Assess for Plasmodium parasites.
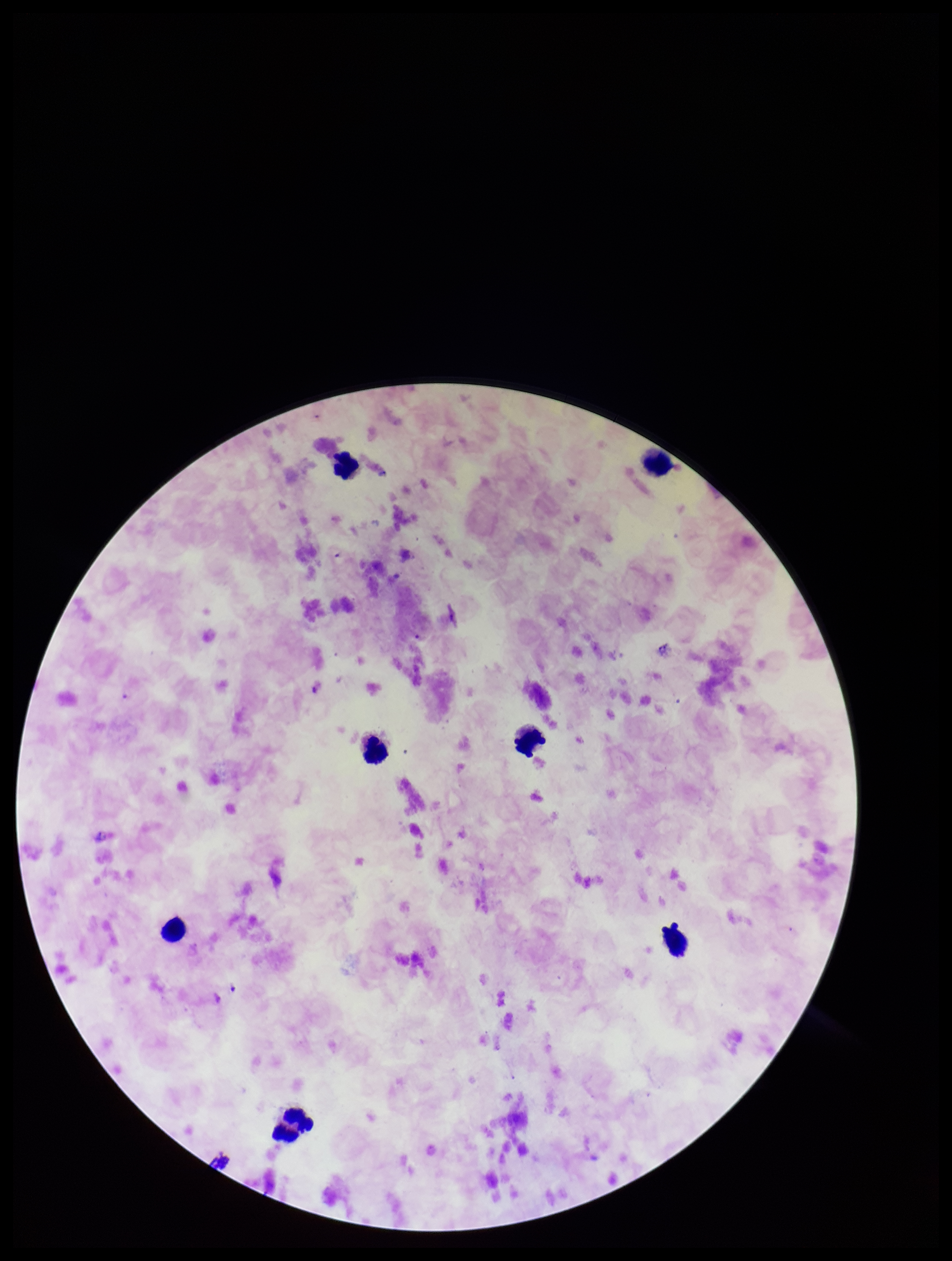

None identified.

Summary:
  - Capture: smartphone photograph through the microscope eyepiece
  - Patient malaria status: infected
  - Parasite count: 0
  - Stain: Giemsa
  - Leukocyte count: 7
  - Field of view: one from this slide
  - Image size: 952×1261 pixels
  - Preparation: thick blood smear
  - Species reported for this patient: Plasmodium falciparum